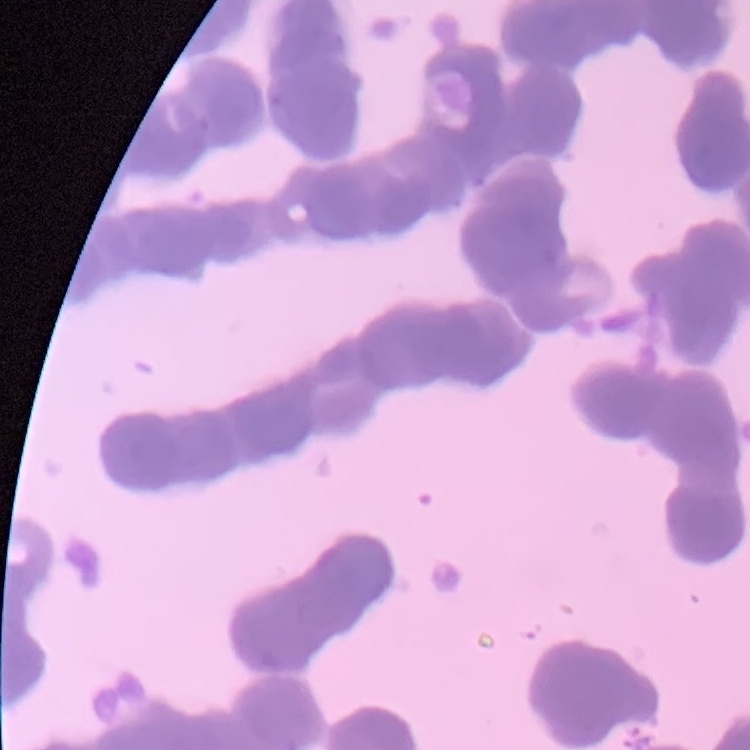 The red blood cells exhibit rouleaux formation. Stained with either Field's or Giemsa. One tile cut from a larger photomicrograph. Thin blood smear.